Locate and identify every blood parasite.
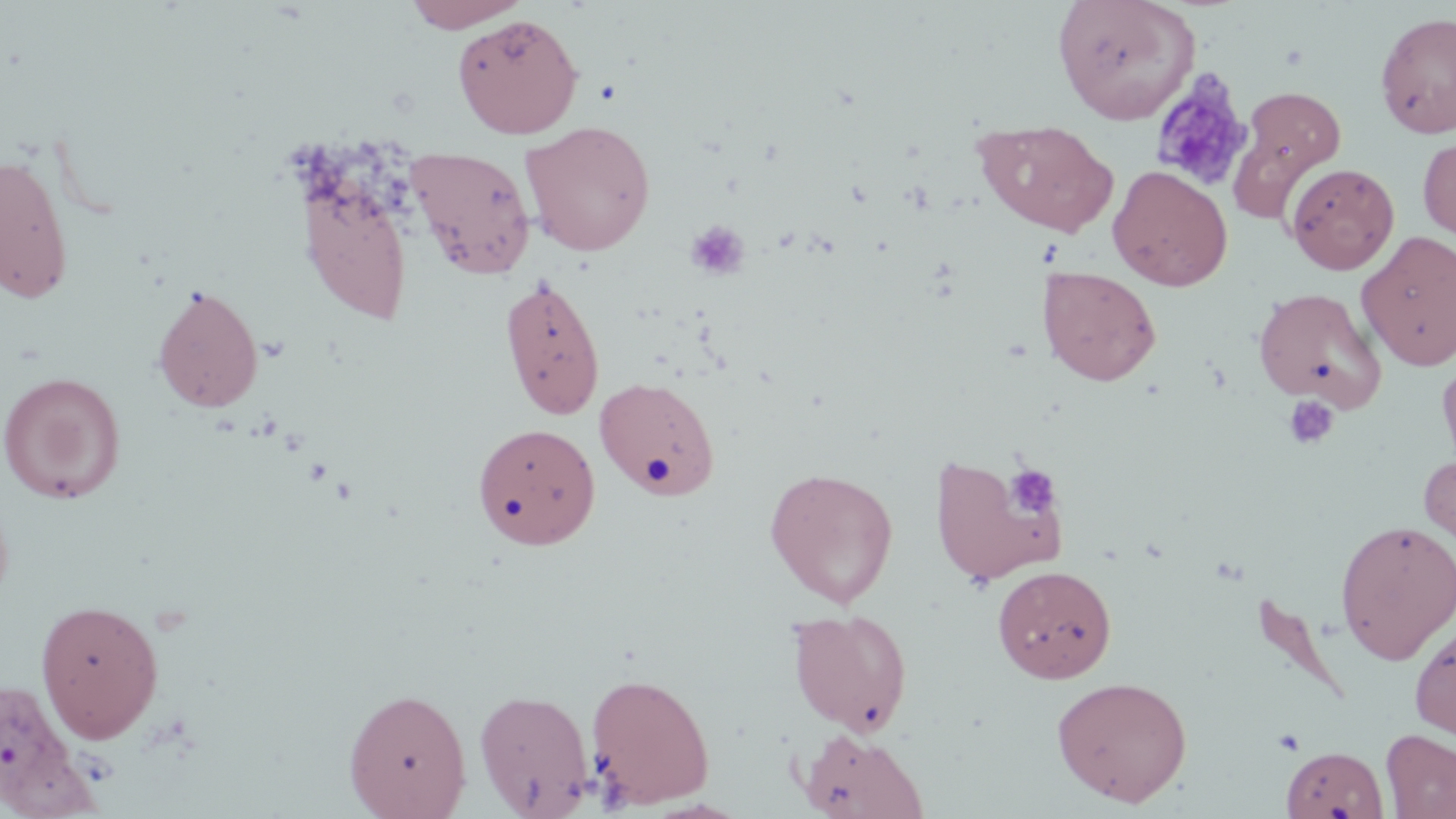
No blood parasites seen.

slide_level_diagnosis: negative for blood parasites
stain: May-Grünwald-Giemsa
modality: light microscopy
platelet_locations: 'approximate bounding boxes as (x1, y1, x2, y2) in pixels: (1150, 70, 1255, 192), (686, 219, 751, 281), (1282, 396, 1339, 450), (1006, 465, 1061, 519), (1272, 728, 1305, 755)'
magnification: 1000x
image_size: 1456×819 pixels
field_of_view: one of a larger specimen
uninfected_red_blood_cell_locations: 'approximate bounding boxes as (x1, y1, x2, y2) in pixels: (403, 0, 531, 32), (1053, 0, 1199, 124), (1375, 11, 1456, 139), (452, 14, 584, 139), (1232, 87, 1346, 208), (974, 119, 1119, 237), (520, 120, 656, 256), (1418, 137, 1456, 241), (405, 145, 537, 279), (0, 149, 74, 306), (1285, 163, 1399, 274), (1108, 165, 1233, 291), (298, 179, 414, 325), (1358, 231, 1456, 371), (1038, 265, 1161, 385), (498, 273, 606, 420), (151, 284, 264, 414), (1254, 287, 1385, 411), (1437, 358, 1456, 474), (0, 371, 126, 504), (594, 375, 721, 501), (472, 423, 600, 549), (1418, 451, 1456, 563), (929, 453, 1065, 585), (764, 466, 899, 607), (1335, 519, 1455, 664), (992, 565, 1117, 683), (35, 598, 165, 742), (787, 608, 913, 735), (1410, 622, 1456, 742), (585, 671, 716, 809), (1051, 676, 1193, 806), (0, 678, 84, 811), (343, 687, 472, 818), (474, 687, 594, 817), (798, 729, 929, 819), (1380, 729, 1455, 818), (1281, 745, 1387, 819)'
preparation: thin blood film